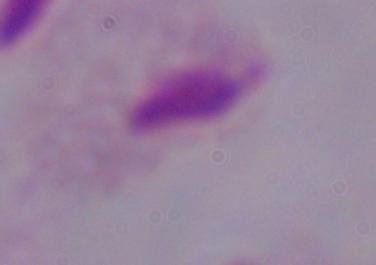

{
  "identification": "trichomonad",
  "magnification": "1000x",
  "modality": "micrograph"
}